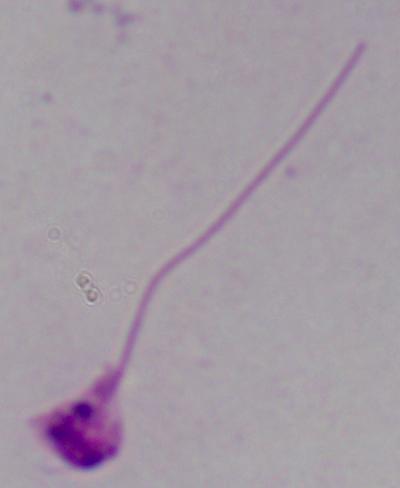

modality = photomicrograph
magnification = 1000x
identification = Leishmania